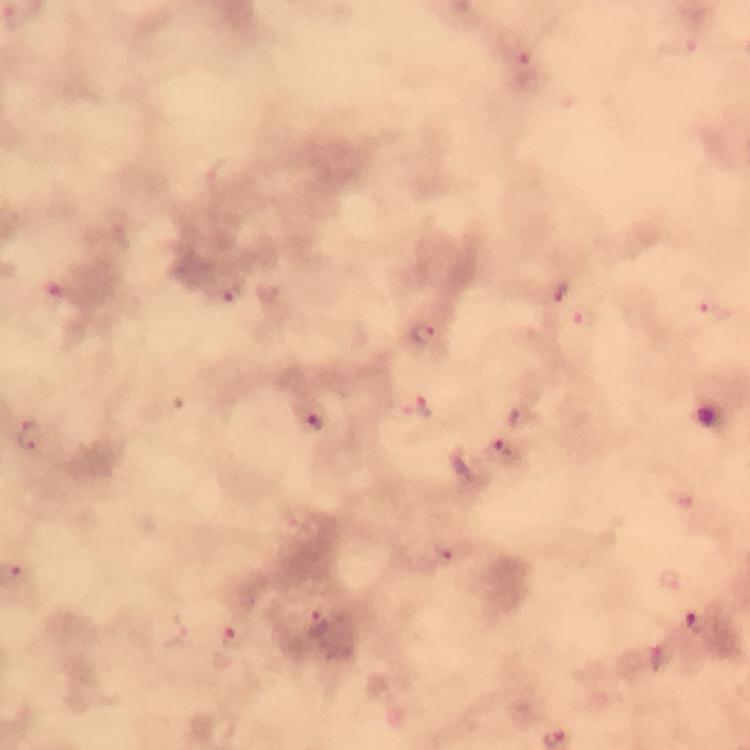

Approximate object centers, in pixels from the top-left corner. Plasmodium parasite locations: (x=524, y=49), (x=560, y=292), (x=231, y=294), (x=61, y=296), (x=715, y=311), (x=583, y=318), (x=423, y=333), (x=420, y=407), (x=317, y=422), (x=32, y=436), (x=506, y=449), (x=450, y=551), (x=670, y=579), (x=320, y=622), (x=698, y=622), (x=233, y=636), (x=663, y=655). Giemsa-stained preparation. Thick blood film. Immersion oil applied. A crop from one field of view. Photographed through the microscope with a smartphone camera. From a diagnostic examination for malaria. Image is 750×750 pixels. At 100x magnification.